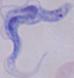
Micrograph. 1000x magnification. A trypanosome is seen.